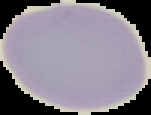

Summary:
  - Image size: 151×115 pixels
  - Image type: segmented cell region on a black background
  - Result: no Plasmodium parasites detected
  - Preparation: thin blood film